Give the extent of all uninfected red blood cells.
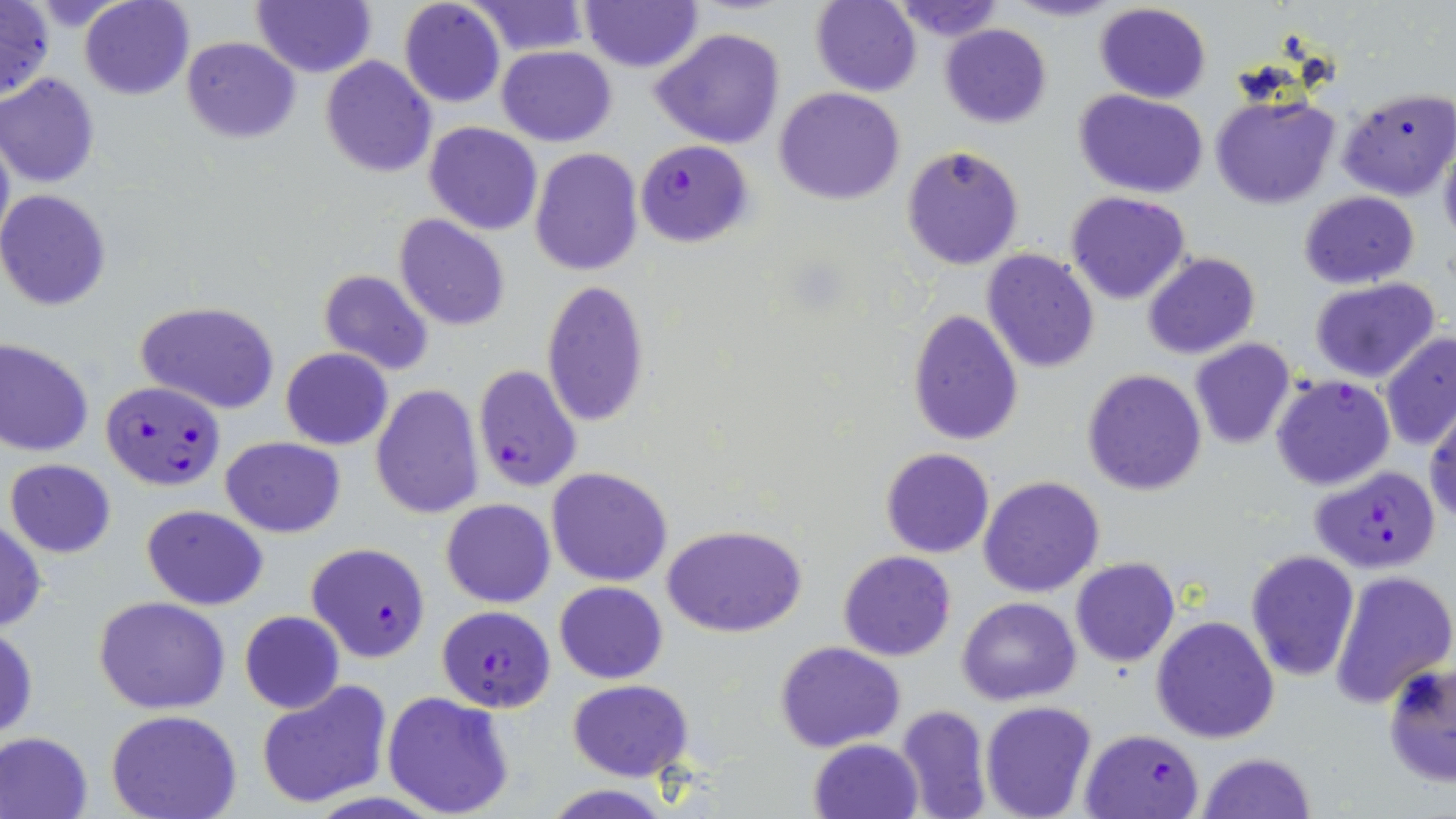

Approximate bounding boxes as named x1/y1/x2/y2 corners in pixels.
Uninfected red blood cells: (x1=80, y1=0, x2=194, y2=100), (x1=398, y1=0, x2=505, y2=108), (x1=579, y1=0, x2=702, y2=72), (x1=889, y1=0, x2=1004, y2=39), (x1=1007, y1=0, x2=1121, y2=23), (x1=0, y1=1, x2=54, y2=104), (x1=252, y1=1, x2=376, y2=77), (x1=466, y1=1, x2=590, y2=56), (x1=810, y1=1, x2=923, y2=96), (x1=1093, y1=2, x2=1211, y2=104), (x1=940, y1=24, x2=1051, y2=127), (x1=650, y1=27, x2=786, y2=149), (x1=182, y1=36, x2=300, y2=142), (x1=496, y1=46, x2=617, y2=145), (x1=320, y1=57, x2=435, y2=177), (x1=0, y1=72, x2=101, y2=187), (x1=1336, y1=86, x2=1453, y2=202), (x1=774, y1=87, x2=905, y2=206), (x1=1075, y1=90, x2=1208, y2=198), (x1=1208, y1=93, x2=1341, y2=210), (x1=424, y1=122, x2=543, y2=235), (x1=0, y1=128, x2=14, y2=253), (x1=1438, y1=136, x2=1456, y2=247), (x1=901, y1=144, x2=1025, y2=270), (x1=530, y1=148, x2=642, y2=277), (x1=0, y1=190, x2=115, y2=311), (x1=1297, y1=191, x2=1419, y2=289), (x1=1065, y1=192, x2=1191, y2=305), (x1=394, y1=215, x2=510, y2=331), (x1=980, y1=248, x2=1102, y2=374), (x1=1142, y1=252, x2=1261, y2=360), (x1=318, y1=269, x2=433, y2=376), (x1=1308, y1=278, x2=1441, y2=384), (x1=540, y1=279, x2=651, y2=427), (x1=136, y1=301, x2=280, y2=414), (x1=907, y1=308, x2=1024, y2=445), (x1=1379, y1=332, x2=1456, y2=450), (x1=0, y1=338, x2=96, y2=457), (x1=1188, y1=338, x2=1296, y2=450), (x1=281, y1=347, x2=393, y2=449), (x1=1081, y1=368, x2=1207, y2=497), (x1=371, y1=384, x2=483, y2=518), (x1=1426, y1=405, x2=1456, y2=527), (x1=220, y1=436, x2=346, y2=537), (x1=881, y1=446, x2=996, y2=559), (x1=5, y1=457, x2=116, y2=558), (x1=546, y1=467, x2=673, y2=586), (x1=978, y1=475, x2=1105, y2=598), (x1=442, y1=499, x2=555, y2=607), (x1=141, y1=504, x2=267, y2=609), (x1=0, y1=518, x2=47, y2=631), (x1=664, y1=524, x2=805, y2=638), (x1=838, y1=550, x2=956, y2=661), (x1=1244, y1=550, x2=1361, y2=680), (x1=1070, y1=558, x2=1180, y2=668), (x1=1328, y1=569, x2=1456, y2=707), (x1=555, y1=581, x2=668, y2=683), (x1=94, y1=596, x2=231, y2=714), (x1=957, y1=596, x2=1081, y2=705), (x1=240, y1=610, x2=345, y2=713), (x1=1151, y1=615, x2=1280, y2=742), (x1=1, y1=623, x2=38, y2=743), (x1=776, y1=641, x2=905, y2=752), (x1=1382, y1=661, x2=1456, y2=788), (x1=256, y1=680, x2=393, y2=809), (x1=568, y1=680, x2=694, y2=781), (x1=382, y1=690, x2=514, y2=817), (x1=980, y1=702, x2=1098, y2=819), (x1=895, y1=703, x2=992, y2=818), (x1=106, y1=710, x2=243, y2=819), (x1=0, y1=730, x2=95, y2=818), (x1=810, y1=738, x2=922, y2=818), (x1=1197, y1=751, x2=1317, y2=819), (x1=543, y1=785, x2=673, y2=818).

Plasmodium falciparum-infected red blood cell locations: (x1=634, y1=140, x2=754, y2=250), (x1=472, y1=365, x2=583, y2=492), (x1=1270, y1=375, x2=1396, y2=491), (x1=101, y1=381, x2=225, y2=491), (x1=1307, y1=464, x2=1442, y2=574), (x1=305, y1=541, x2=432, y2=663), (x1=437, y1=605, x2=556, y2=712), (x1=1080, y1=729, x2=1205, y2=819). Slide-level diagnosis: Plasmodium falciparum. Image is 1456×819 pixels. Optical microscopy. Thin blood film. One field of a larger specimen. Captured at 1000x magnification. May-Grünwald-Giemsa-stained preparation.